Classify this cell by malaria status.
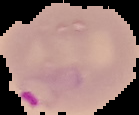
Parasitized.

Summary:
  - Preparation: thin blood film
  - Image size: 139×115 pixels
  - Image type: segmented cell region with the area outside set to black